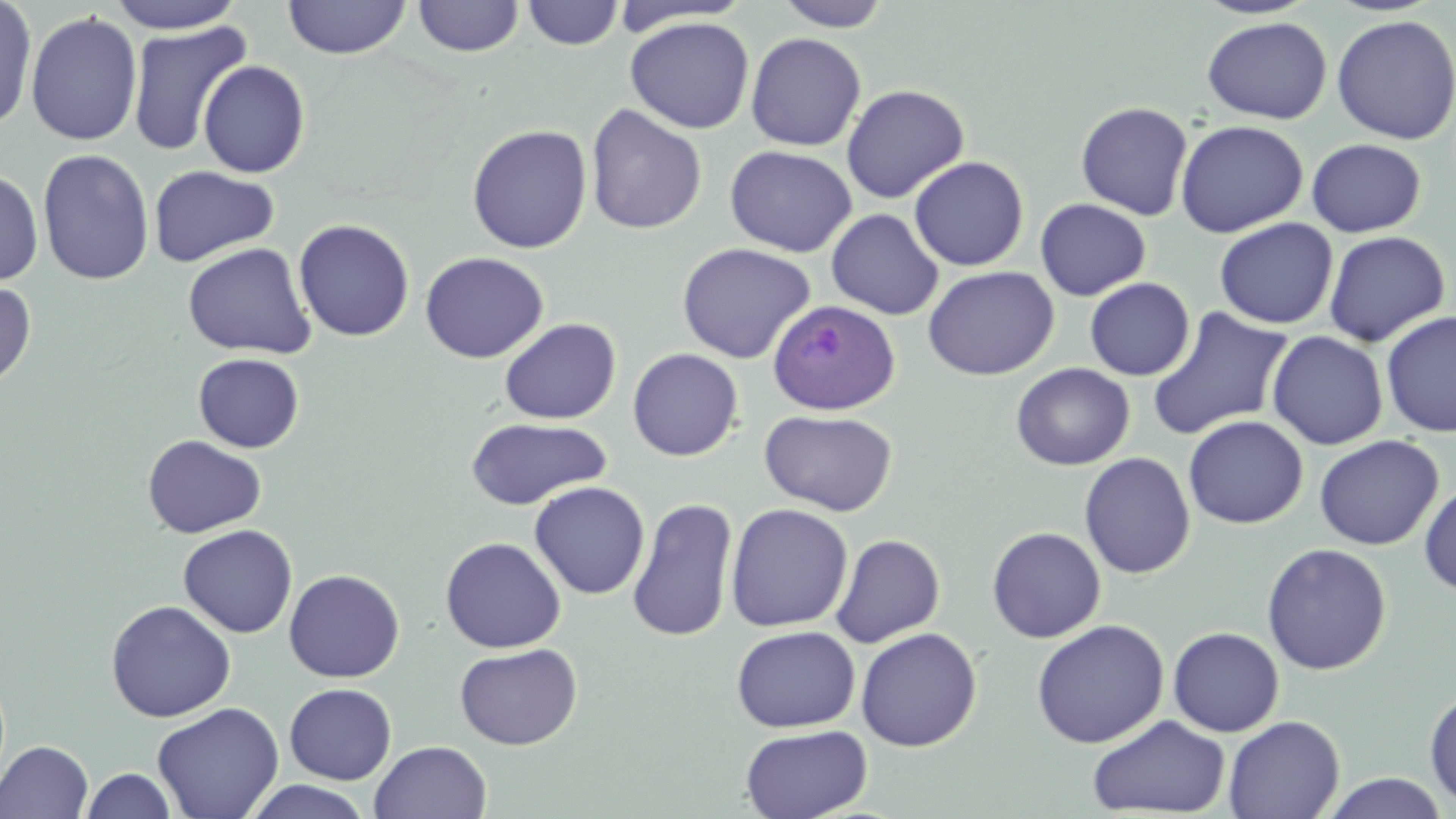 Approximate bounding boxes as (x1, y1, x2, y2) in pixels. Uninfected red blood cell locations: (0, 0, 37, 131), (105, 0, 249, 34), (283, 0, 411, 59), (412, 0, 525, 57), (522, 1, 623, 49), (774, 1, 895, 31), (25, 11, 143, 147), (1330, 14, 1456, 145), (625, 16, 755, 134), (1201, 16, 1332, 124), (127, 20, 251, 156), (745, 33, 866, 151), (196, 59, 310, 178), (840, 84, 969, 203), (1075, 101, 1193, 221), (585, 104, 707, 235), (1175, 120, 1309, 238), (466, 124, 593, 254), (1305, 138, 1426, 238), (725, 145, 857, 257), (37, 148, 154, 285), (909, 156, 1029, 272), (148, 166, 280, 267), (0, 168, 44, 286), (1035, 198, 1151, 301), (826, 208, 943, 320), (293, 218, 415, 341), (1213, 218, 1338, 329), (1322, 231, 1451, 347), (182, 242, 316, 359), (676, 242, 816, 364), (420, 251, 549, 364), (923, 265, 1059, 381), (1085, 278, 1195, 381), (0, 279, 37, 390), (1147, 306, 1294, 441), (1380, 310, 1456, 437), (498, 317, 621, 424), (1266, 331, 1388, 449), (627, 348, 743, 461), (192, 352, 305, 453), (1011, 363, 1134, 470), (760, 409, 898, 516), (465, 415, 614, 510), (1183, 415, 1308, 529), (142, 434, 267, 539), (1313, 435, 1444, 550), (1079, 452, 1195, 579), (528, 481, 650, 600), (1419, 482, 1456, 597), (626, 498, 739, 642), (725, 503, 853, 633), (178, 524, 298, 638), (986, 526, 1106, 643), (831, 533, 946, 647), (440, 536, 566, 653), (1261, 542, 1392, 675), (284, 568, 405, 683), (105, 599, 236, 722), (1031, 619, 1169, 749), (730, 625, 860, 732), (1167, 626, 1284, 737), (855, 627, 982, 752), (454, 643, 582, 750), (284, 683, 397, 784), (1424, 687, 1456, 808), (152, 702, 284, 819), (1087, 714, 1231, 817), (1223, 715, 1344, 819), (740, 724, 872, 819), (0, 740, 94, 818), (369, 740, 492, 819), (80, 767, 179, 818), (1319, 772, 1450, 818), (241, 780, 375, 819). Plasmodium ovale-infected red blood cell locations: (767, 299, 900, 415). Slide-level diagnosis: Plasmodium ovale. May-Grünwald-Giemsa-stained preparation. Light microscopy. Thin blood smear. Image is 1456×819 pixels. Single field of view. Captured at 1000x magnification.